Assess this cell for malaria.
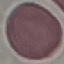
It is uninfected.

Summary:
  - Image type: automatically extracted cell patch, resized to 64 × 64 pixels
  - Stain: Giemsa
  - Preparation: thin blood film
  - Capture: smartphone camera at the microscope eyepiece